Assess the morphology of the red blood cells.
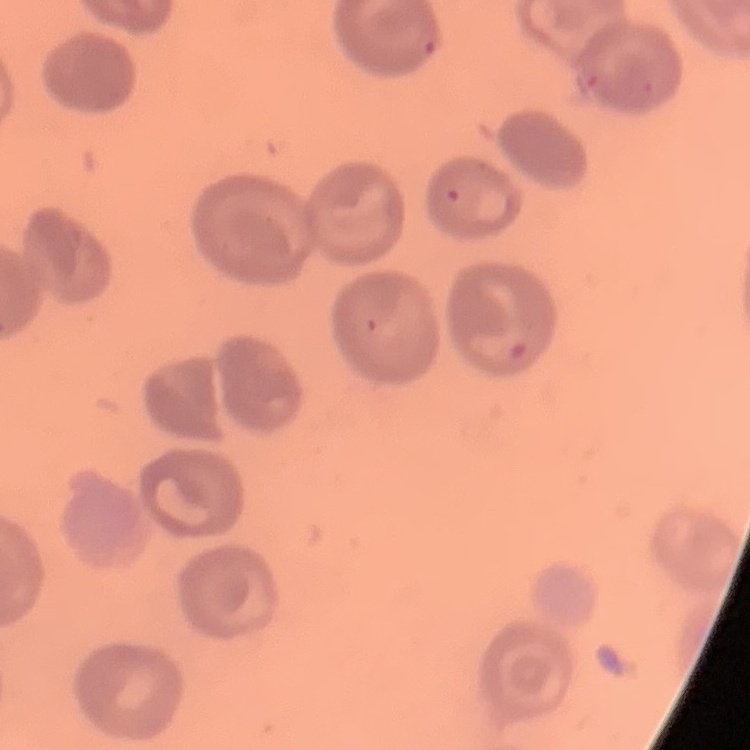
They show no rouleaux formation.

Summary:
  - Image type: one tile cut from a larger photomicrograph
  - Preparation: thin blood smear
  - Stain: Field's or Giemsa